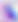
modality = micrograph
identification = Toxoplasma gondii
magnification = 400x